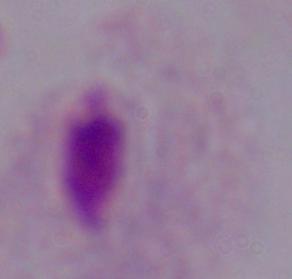 Captured at 1000x magnification. A trichomonad is seen. Photomicrograph.